Assess this cell for malaria.
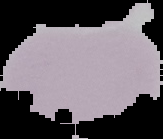
It is uninfected.

{
  "image_size": "163×139 pixels",
  "preparation": "thin blood film",
  "image_type": "segmented cell region with the area outside set to black"
}